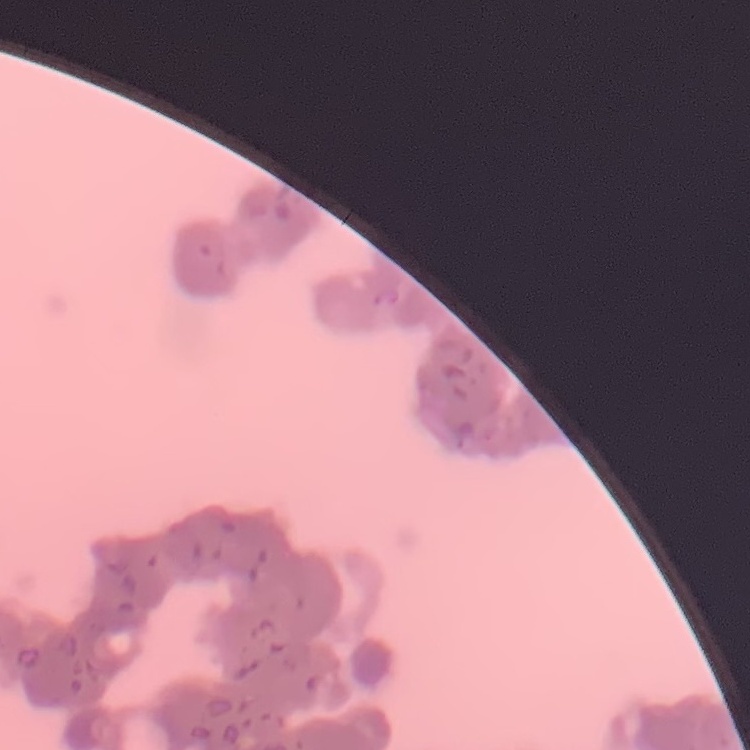
red blood cell morphology = rouleaux formation
preparation = thin blood film
stain = Field's or Giemsa
image type = one tile cut from a larger photomicrograph